Classify this cell by malaria status.
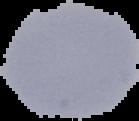

It is uninfected.

image size = 139×121 pixels
image type = cell region segmented out of the field of view; surrounding area masked to black
preparation = thin blood film